State which cell type is depicted.
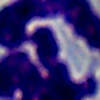

A leukocyte.

modality: photomicrograph
magnification: 1000x